Name the parasite shown.
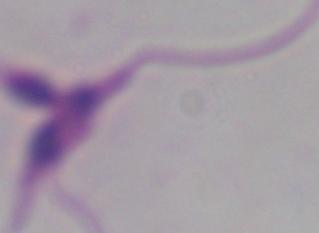
This is Leishmania.

{
  "modality": "micrograph",
  "magnification": "1000x"
}